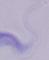

Summary:
  - Identification: trypanosome
  - Magnification: 1000x
  - Modality: photomicrograph